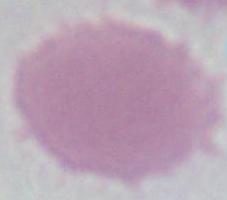
Summary:
  - Identification: erythrocyte
  - Magnification: 1000x
  - Modality: photomicrograph